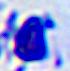
{
  "identification": "leukocyte",
  "magnification": "400x",
  "modality": "photomicrograph"
}